Identify the cell.
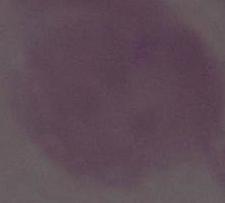
An erythrocyte.

Summary:
  - Modality: photomicrograph
  - Magnification: 1000x